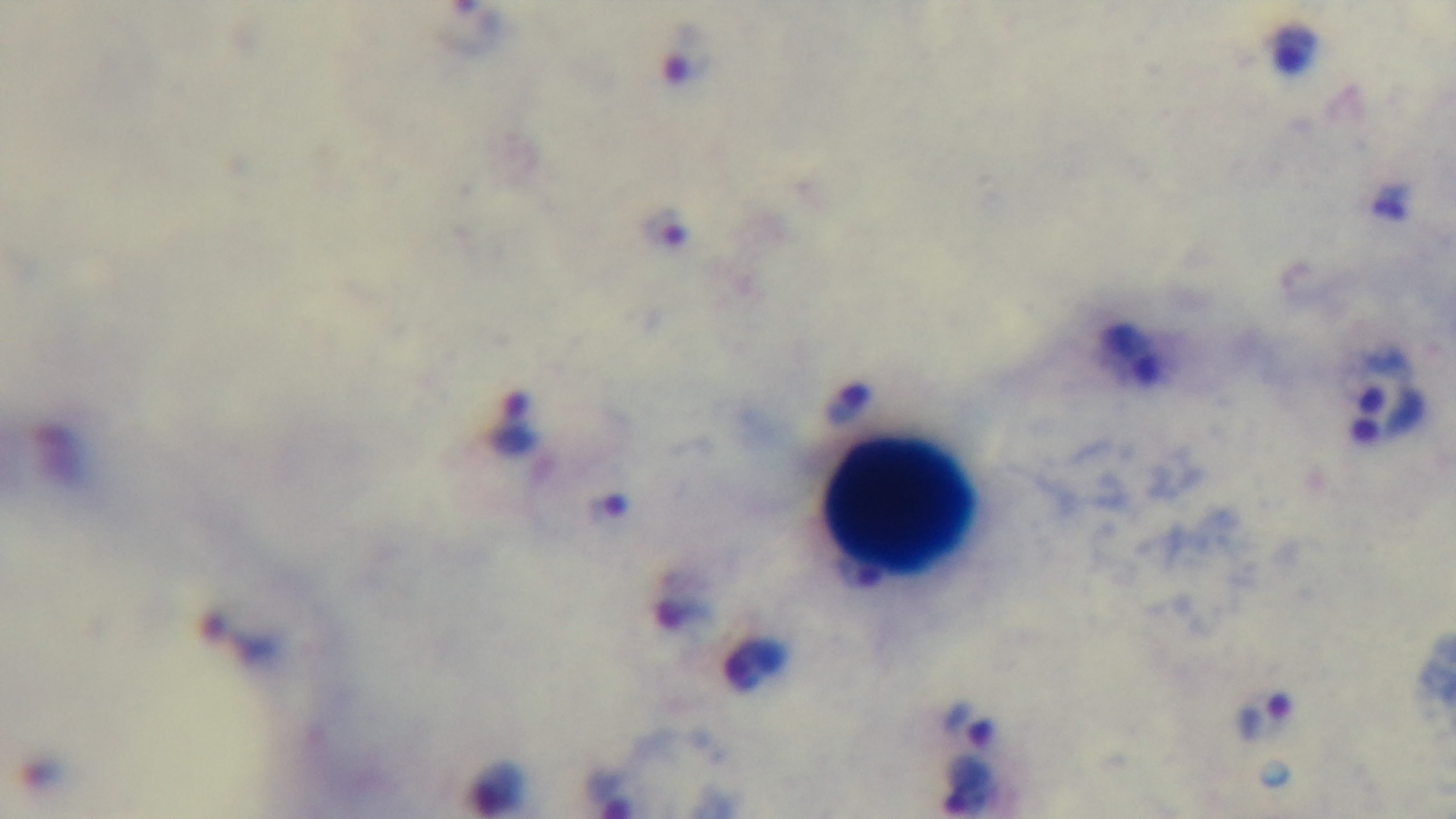

field of view = single
modality = light microscopy
malaria status = infected
stain = Giemsa
objective = 100x oil immersion
capture = mounted 4K digital camera
preparation = thick smear